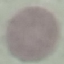 Malaria status: uninfected. Giemsa-stained preparation. Photographed with a smartphone camera at the microscope eyepiece. Cell patch, automatically extracted from a larger field of view and resized to 64 × 64 pixels. Thin blood smear.